Locate every blood parasite and identify its species.
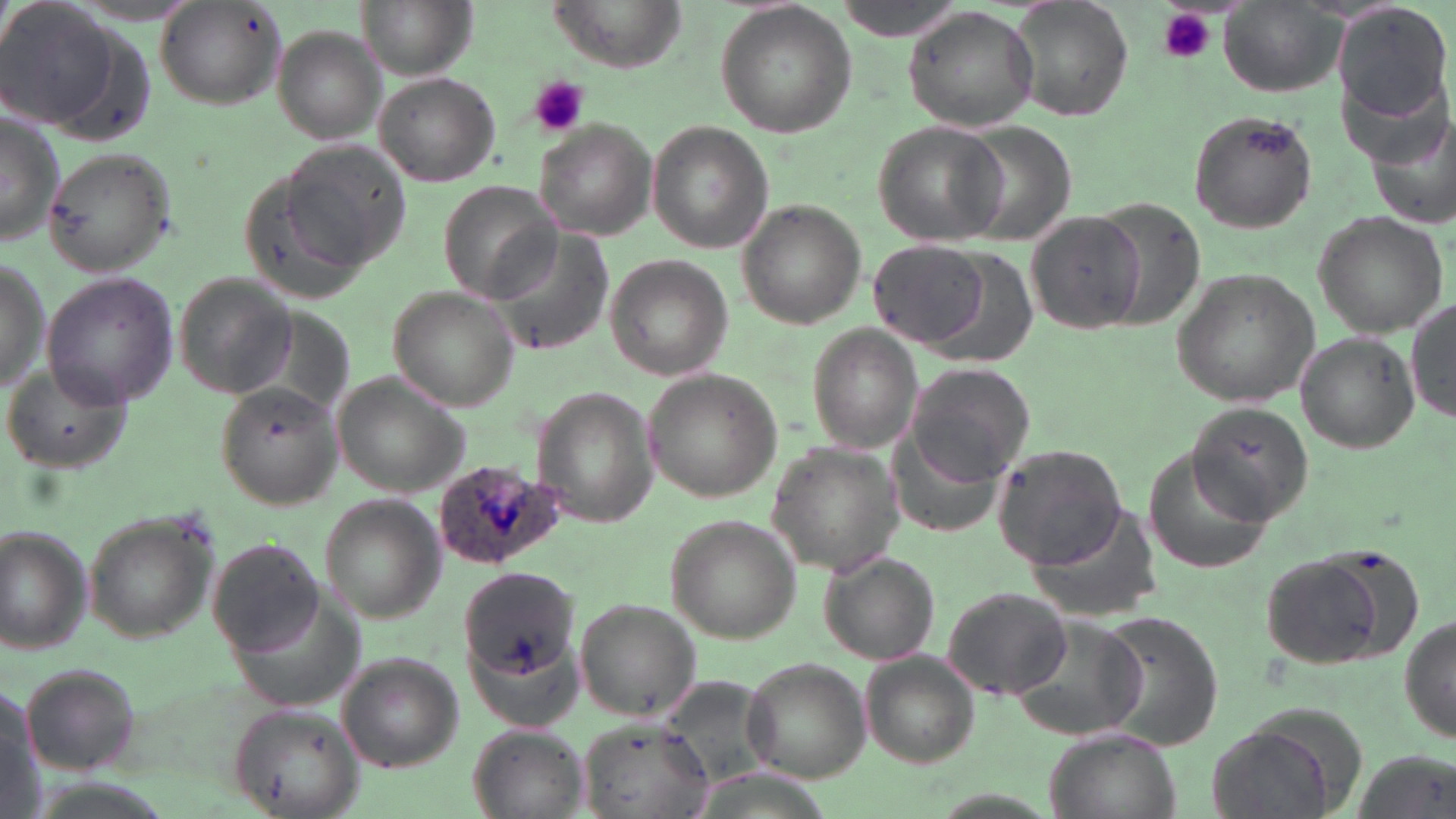
Approximate bounding boxes as [x1, y1, x2, y2] in pixels.
Plasmodium ovale-infected red blood cells: [435, 459, 563, 571].
No Plasmodium falciparum, Plasmodium malariae, Plasmodium vivax, Babesia divergens, or Trypanosoma brucei observed.

Uninfected red blood cell locations: [0, 0, 121, 130], [359, 0, 474, 81], [543, 0, 686, 73], [828, 0, 969, 38], [1004, 0, 1135, 122], [152, 1, 287, 112], [1220, 3, 1343, 97], [715, 4, 857, 139], [1334, 6, 1452, 126], [903, 8, 1036, 133], [272, 25, 385, 143], [374, 71, 499, 187], [1187, 108, 1317, 235], [0, 113, 66, 245], [872, 120, 1005, 245], [535, 121, 657, 239], [950, 121, 1078, 245], [647, 123, 771, 253], [279, 136, 410, 269], [43, 146, 174, 275], [239, 172, 372, 305], [439, 181, 557, 300], [1095, 198, 1206, 333], [739, 200, 865, 328], [1313, 212, 1449, 336], [480, 213, 614, 352], [1026, 213, 1146, 336], [868, 240, 989, 349], [922, 247, 1037, 369], [603, 253, 732, 382], [0, 255, 47, 392], [1172, 269, 1320, 406], [172, 271, 297, 398], [43, 272, 180, 406], [388, 288, 517, 409], [1406, 299, 1455, 424], [222, 306, 354, 434], [808, 324, 924, 454], [1293, 333, 1420, 454], [907, 361, 1039, 484], [6, 363, 128, 474], [643, 370, 781, 500], [333, 373, 470, 495], [215, 383, 345, 509], [532, 388, 658, 528], [1187, 400, 1315, 522], [884, 406, 1003, 537], [767, 441, 903, 575], [993, 444, 1129, 568], [1144, 453, 1278, 574], [319, 496, 442, 623], [1031, 502, 1160, 619], [82, 507, 221, 643], [667, 515, 804, 643], [0, 526, 93, 653], [206, 538, 329, 657], [1255, 550, 1414, 671], [819, 551, 941, 665], [458, 569, 576, 679], [226, 576, 365, 714], [940, 585, 1072, 699], [576, 599, 702, 721], [1093, 609, 1224, 748], [1399, 612, 1454, 747], [1012, 617, 1148, 741], [461, 629, 591, 735], [862, 653, 979, 766], [336, 654, 463, 771], [743, 658, 874, 782], [20, 660, 144, 775], [653, 676, 779, 791], [0, 677, 40, 815], [234, 702, 361, 818], [578, 716, 713, 819], [467, 724, 589, 819], [1206, 725, 1334, 819], [1046, 730, 1177, 819]. Platelet locations: [1157, 5, 1216, 65], [528, 76, 589, 137]. Slide-level diagnosis: Plasmodium ovale. Image is 1456×819 pixels. One field of a larger specimen. Thin blood smear. May-Grünwald-Giemsa stain. 1000x magnification. Light microscopy.